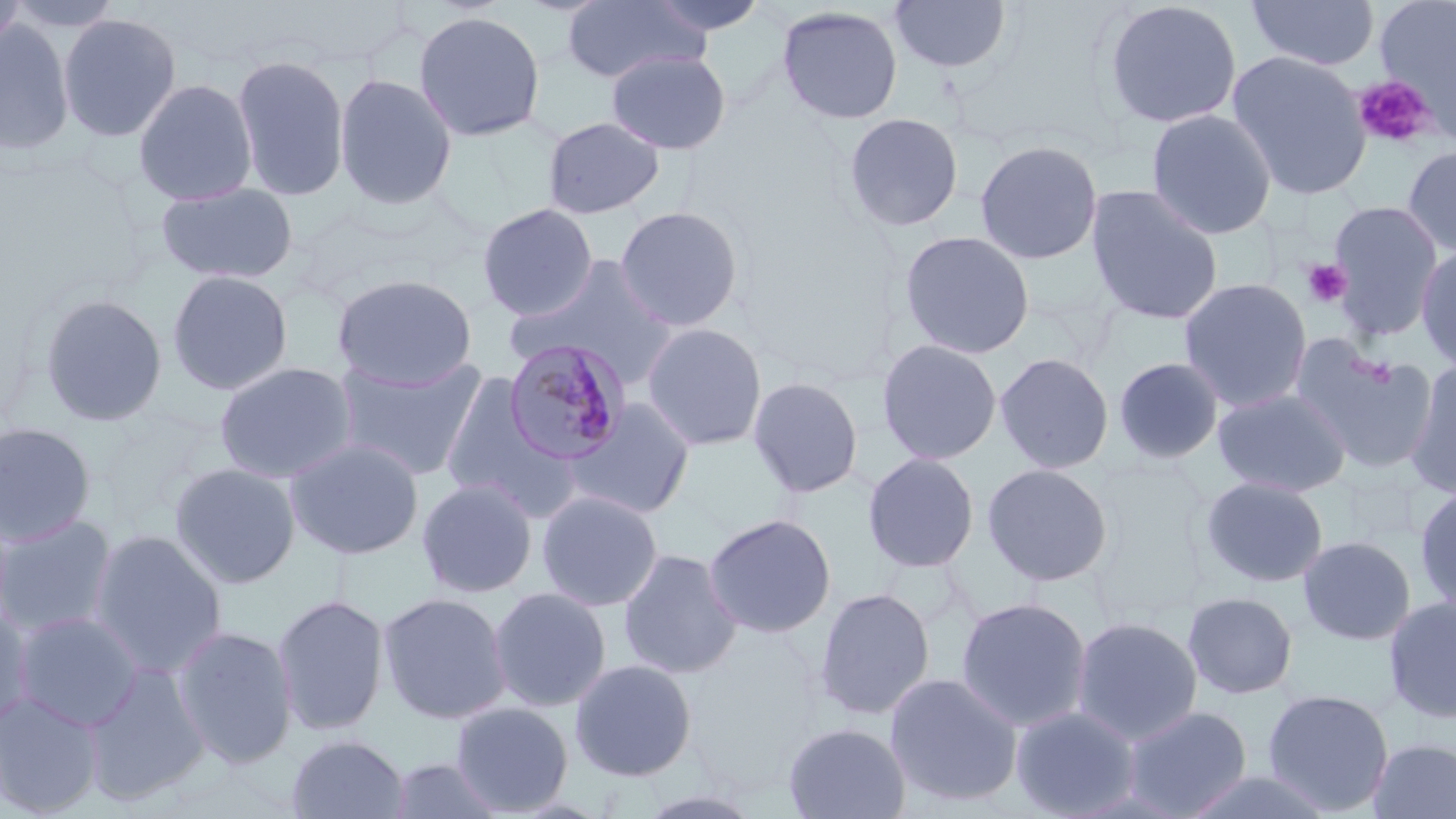

Approximate bounding boxes as [x1, y1, x2, y2] in pixels. Platelet locations: [1352, 74, 1437, 149], [1302, 258, 1352, 308], [1358, 356, 1395, 387]. Uninfected red blood cell locations: [0, 0, 30, 59], [561, 0, 711, 85], [642, 0, 770, 37], [889, 0, 1012, 75], [1101, 0, 1243, 129], [1246, 0, 1380, 71], [1375, 0, 1456, 131], [777, 5, 903, 125], [413, 9, 546, 143], [58, 12, 182, 143], [0, 21, 75, 155], [606, 49, 731, 155], [1227, 50, 1372, 201], [231, 54, 351, 202], [334, 72, 457, 210], [132, 77, 258, 206], [1146, 108, 1277, 240], [843, 112, 965, 232], [542, 116, 665, 219], [974, 139, 1104, 265], [1401, 143, 1456, 258], [156, 182, 299, 284], [1085, 184, 1224, 325], [1327, 200, 1445, 339], [477, 203, 599, 321], [613, 205, 745, 331], [898, 230, 1035, 359], [1416, 245, 1456, 374], [509, 256, 679, 387], [167, 269, 294, 396], [331, 274, 478, 389], [1178, 277, 1313, 413], [38, 292, 168, 427], [641, 322, 768, 451], [876, 338, 1003, 466], [1292, 340, 1437, 475], [994, 352, 1115, 474], [334, 355, 488, 481], [1112, 356, 1225, 464], [214, 361, 359, 484], [1403, 361, 1456, 498], [438, 372, 578, 522], [747, 376, 864, 500], [1212, 387, 1352, 497], [562, 397, 696, 520], [0, 421, 98, 547], [285, 437, 424, 560], [862, 452, 980, 574], [169, 461, 302, 589], [982, 462, 1114, 587], [1341, 469, 1421, 543], [1199, 475, 1329, 588], [416, 477, 538, 598], [1415, 484, 1456, 614], [536, 490, 664, 612], [0, 504, 16, 634], [0, 513, 118, 639], [702, 513, 837, 638], [88, 528, 228, 678], [1298, 535, 1416, 646], [617, 548, 743, 679], [487, 587, 612, 712], [813, 587, 936, 720], [378, 591, 511, 725], [1182, 591, 1299, 700], [272, 593, 391, 736], [1383, 594, 1456, 725], [954, 596, 1092, 732], [0, 605, 35, 730], [12, 610, 145, 731], [1071, 615, 1203, 745], [171, 625, 299, 769], [569, 658, 698, 781], [81, 661, 211, 805], [884, 672, 1024, 808], [1262, 689, 1395, 815], [0, 691, 104, 817], [450, 701, 574, 815], [1010, 705, 1141, 818], [1120, 705, 1253, 818], [783, 721, 911, 819], [286, 733, 410, 819], [1365, 737, 1456, 819], [387, 758, 506, 818], [1176, 768, 1342, 819], [631, 786, 767, 818]. Plasmodium malariae-infected red blood cell locations: [501, 339, 633, 467]. Slide-level diagnosis: Plasmodium malariae. Image is 1456×819 pixels. Light microscopy. May-Grünwald-Giemsa-stained preparation. One field of a larger specimen. 1000x magnification. Thin blood smear.